Name the parasite shown.
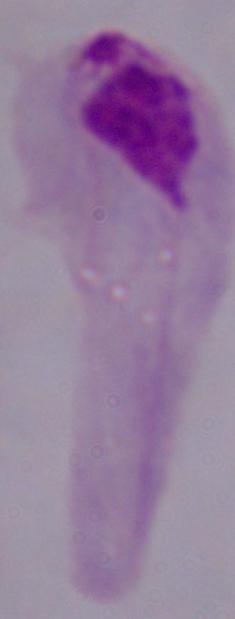
This is a trichomonad.

1000x magnification. Micrograph.